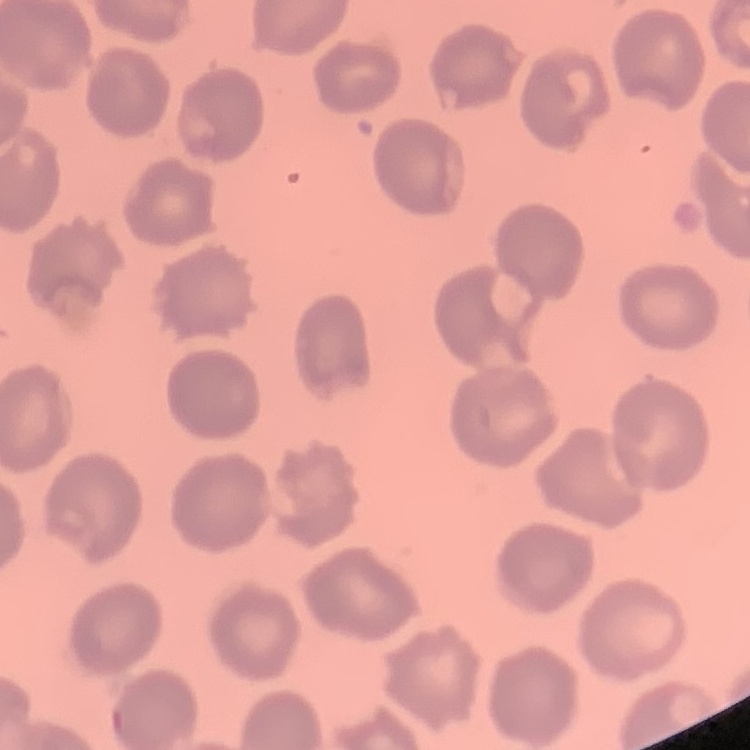
The erythrocytes show no rouleaux formation. Stained with either Field's or Giemsa. Square crop of a larger photomicrograph. Thin peripheral smear.